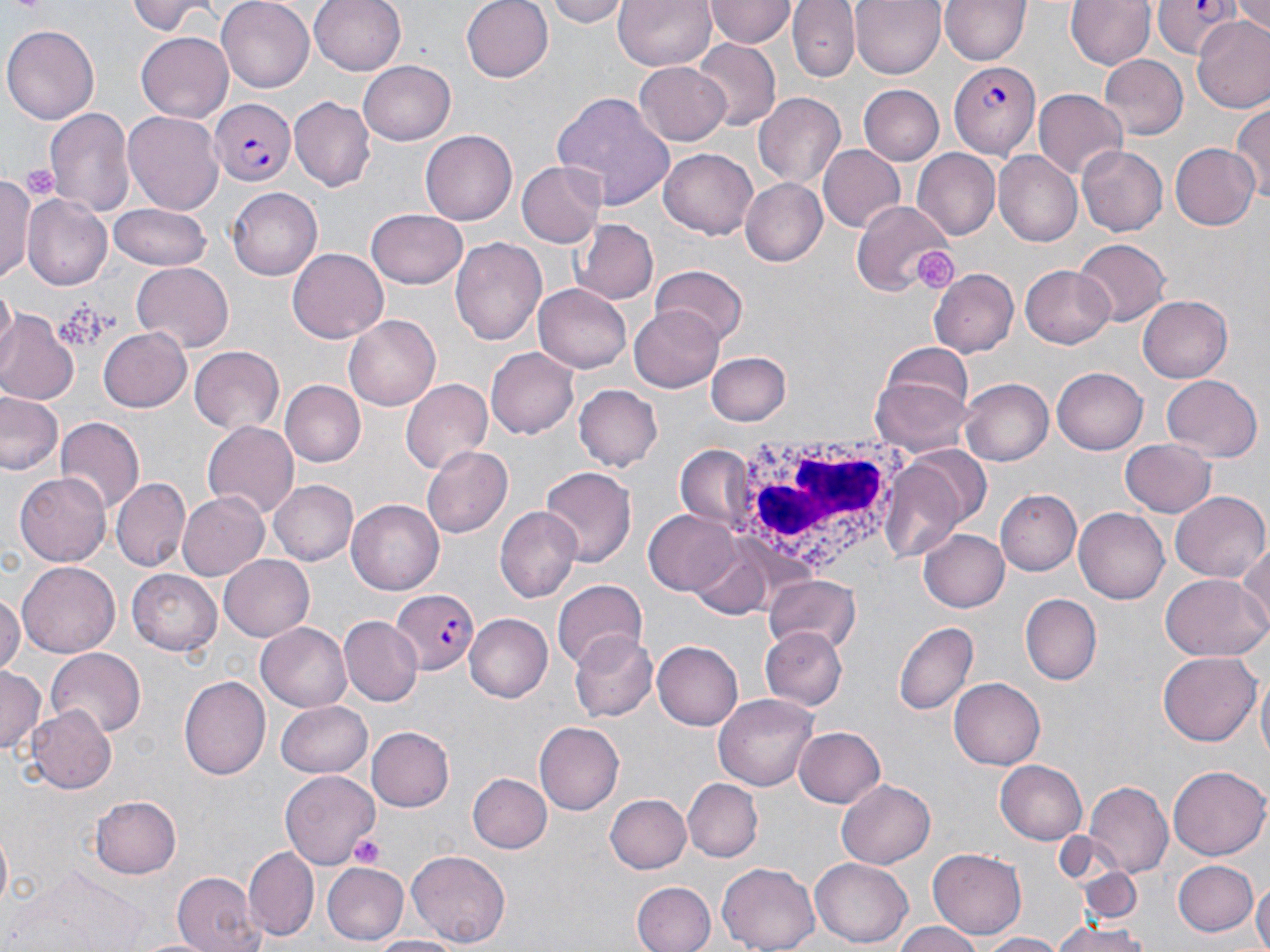

Approximate bounding boxes as [x1, y1, x2, y2] in pixels. Platelet locations: [912, 248, 959, 292], [56, 301, 112, 350], [348, 832, 384, 868]. Uninfected red blood cell locations: [128, 0, 241, 38], [216, 0, 314, 91], [310, 0, 406, 77], [459, 0, 553, 84], [543, 0, 627, 26], [613, 0, 717, 72], [707, 0, 797, 47], [790, 0, 859, 82], [851, 0, 944, 77], [1064, 0, 1156, 70], [938, 1, 1032, 66], [1230, 1, 1270, 40], [1191, 16, 1270, 112], [3, 22, 100, 124], [136, 30, 233, 119], [691, 40, 779, 132], [1098, 55, 1187, 140], [359, 61, 455, 143], [634, 61, 732, 145], [858, 84, 945, 165], [1033, 90, 1127, 182], [753, 92, 845, 189], [550, 93, 676, 210], [289, 97, 375, 190], [1230, 100, 1270, 199], [44, 104, 135, 215], [124, 110, 225, 214], [421, 129, 517, 226], [1169, 143, 1260, 231], [817, 145, 907, 234], [1077, 146, 1166, 237], [659, 148, 758, 240], [913, 150, 1001, 239], [993, 153, 1083, 247], [17, 159, 58, 210], [517, 160, 607, 247], [1, 176, 37, 283], [739, 177, 829, 265], [228, 188, 322, 281], [22, 194, 111, 291], [850, 201, 956, 296], [105, 205, 214, 274], [367, 208, 469, 288], [572, 218, 658, 305], [452, 236, 547, 347], [1075, 239, 1167, 327], [289, 248, 388, 342], [129, 263, 234, 352], [651, 265, 746, 344], [1020, 265, 1118, 348], [929, 267, 1018, 358], [533, 283, 630, 373], [1, 285, 16, 355], [1138, 294, 1232, 383], [631, 307, 723, 393], [0, 312, 78, 407], [342, 315, 440, 412], [99, 324, 192, 412], [878, 340, 975, 429], [485, 345, 579, 440], [190, 346, 287, 433], [708, 352, 791, 426], [1054, 366, 1148, 454], [871, 374, 973, 455], [1163, 375, 1261, 463], [401, 377, 493, 475], [960, 378, 1053, 467], [280, 380, 366, 468], [574, 386, 663, 471], [0, 391, 65, 478], [54, 416, 144, 511], [201, 422, 300, 517], [1121, 438, 1216, 519], [422, 444, 512, 534], [678, 445, 751, 525], [882, 457, 971, 557], [538, 466, 635, 568], [14, 471, 114, 566], [111, 476, 191, 570], [267, 479, 357, 567], [998, 488, 1081, 575], [176, 491, 272, 582], [1171, 491, 1268, 584], [348, 498, 447, 595], [496, 505, 580, 603], [1073, 507, 1170, 604], [644, 510, 739, 595], [919, 530, 1009, 613], [1236, 540, 1270, 632], [686, 541, 781, 619], [219, 554, 316, 640], [19, 561, 119, 657], [129, 568, 225, 655], [1160, 574, 1267, 662], [764, 575, 861, 652], [551, 579, 645, 670], [0, 592, 22, 676], [1021, 596, 1100, 685], [462, 613, 551, 704], [340, 617, 423, 705], [895, 620, 979, 715], [256, 621, 352, 712], [760, 628, 847, 712], [568, 629, 657, 723], [653, 638, 747, 730], [45, 648, 147, 737], [1156, 652, 1260, 745], [0, 666, 44, 756], [179, 675, 270, 779], [1256, 675, 1270, 769], [949, 677, 1046, 769], [712, 693, 819, 793], [275, 701, 372, 778], [29, 705, 115, 793], [534, 721, 624, 816], [366, 726, 454, 813], [793, 726, 887, 807], [994, 760, 1087, 845], [1168, 764, 1269, 860], [282, 769, 376, 869], [470, 773, 550, 854], [836, 777, 937, 870], [682, 778, 762, 862], [1086, 782, 1173, 876], [89, 794, 181, 880], [604, 794, 690, 873], [243, 847, 318, 940], [927, 847, 1026, 942], [408, 849, 510, 948], [811, 858, 913, 948], [1171, 860, 1257, 936], [322, 862, 409, 943], [716, 862, 820, 952], [1081, 868, 1141, 925], [12, 870, 147, 951], [172, 872, 262, 952], [1253, 878, 1270, 952], [631, 881, 715, 952], [1054, 918, 1148, 952], [889, 921, 984, 952], [977, 932, 1072, 952], [368, 934, 469, 952]. White blood cell locations: [720, 429, 915, 580]. Plasmodium falciparum-infected red blood cell locations: [1154, 0, 1241, 59], [947, 59, 1039, 158], [210, 99, 295, 186], [393, 590, 479, 675]. Slide-level diagnosis: Plasmodium falciparum. Thin blood smear. Light microscopy. Single field of view. May-Grünwald-Giemsa stain. Image is 1270×952 pixels. 1000x magnification.